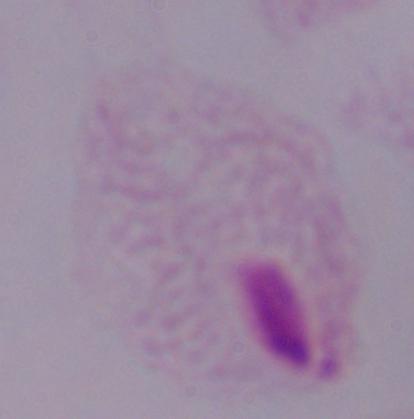
Micrograph. A trichomonad is seen. Captured at 1000x magnification.